Assess this cell for malaria.
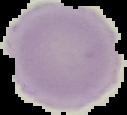
It is uninfected.

preparation: thin blood film
image_type: cell region segmented out of the field of view; surrounding area masked to black
image_size: 127×115 pixels